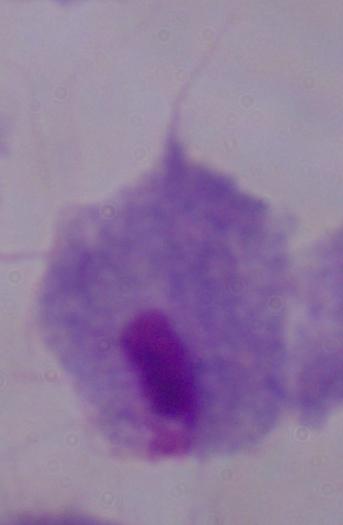

magnification = 1000x
modality = micrograph
identification = trichomonad